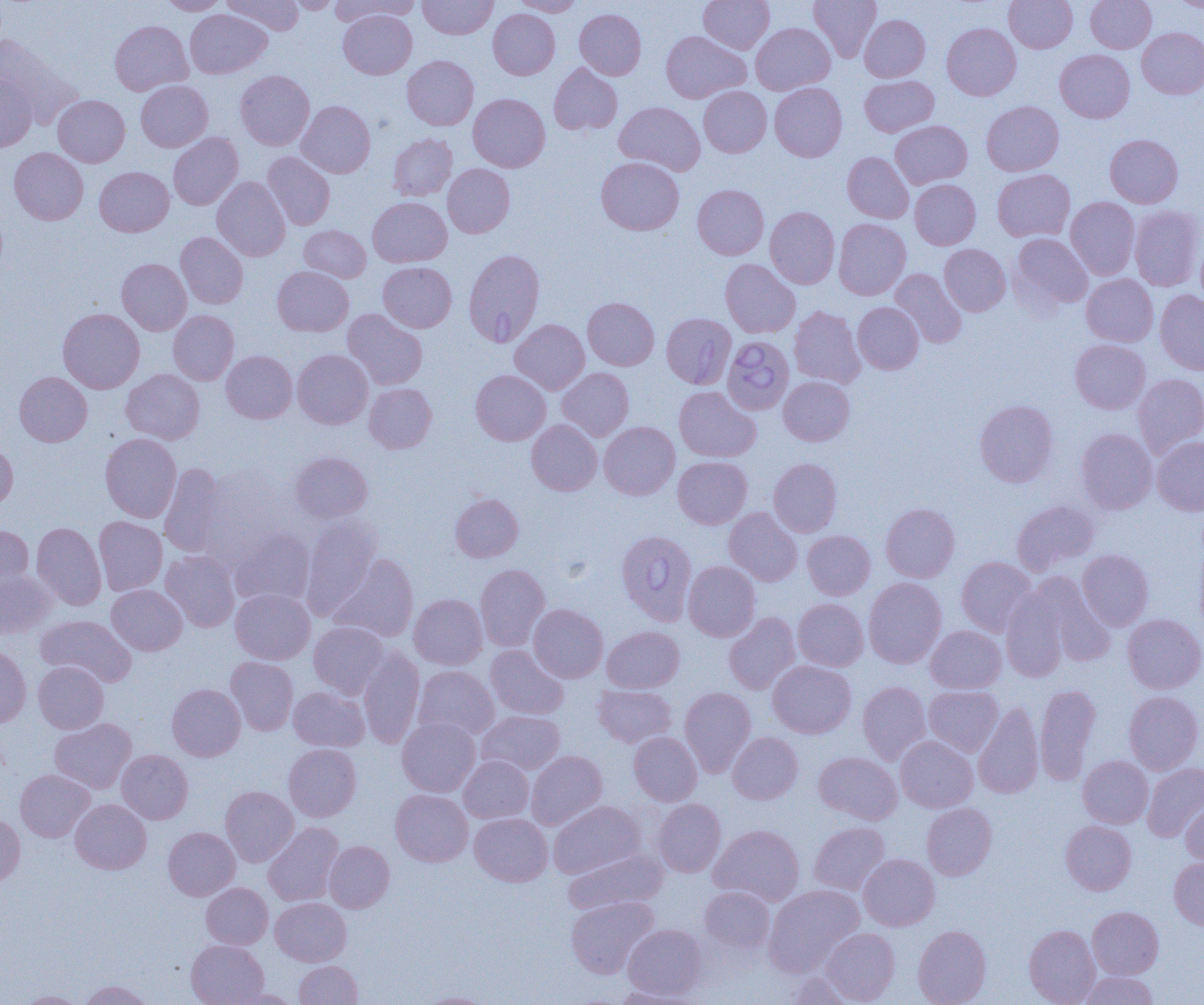
Approximate bounding boxes as [x1, y1, x2, y2] in pixels. Uninfected red blood cell locations: [160, 0, 227, 15], [222, 0, 304, 35], [285, 0, 341, 13], [330, 0, 421, 25], [418, 0, 498, 39], [512, 0, 583, 16], [698, 0, 774, 54], [809, 0, 881, 62], [1004, 0, 1077, 53], [1086, 0, 1156, 53], [1172, 0, 1204, 12], [185, 9, 271, 79], [488, 9, 560, 79], [574, 9, 646, 79], [338, 10, 417, 79], [860, 14, 930, 82], [110, 20, 193, 96], [751, 23, 835, 94], [942, 23, 1021, 100], [1137, 27, 1204, 99], [661, 31, 750, 103], [0, 33, 81, 128], [1055, 49, 1135, 123], [402, 55, 479, 130], [549, 63, 622, 135], [235, 70, 314, 150], [0, 74, 37, 152], [859, 75, 938, 136], [136, 80, 212, 152], [769, 83, 847, 161], [698, 86, 771, 157], [468, 93, 550, 172], [53, 95, 130, 167], [296, 100, 375, 178], [614, 101, 705, 175], [982, 101, 1064, 176], [890, 120, 972, 188], [168, 132, 243, 210], [388, 134, 457, 201], [1105, 134, 1183, 208], [9, 147, 88, 225], [262, 152, 335, 230], [842, 152, 913, 223], [596, 156, 684, 235], [443, 164, 515, 238], [94, 166, 174, 237], [992, 168, 1075, 242], [212, 176, 290, 261], [910, 179, 980, 249], [692, 184, 769, 259], [368, 197, 452, 267], [1066, 197, 1139, 279], [1129, 205, 1203, 291], [765, 206, 840, 289], [833, 218, 910, 300], [299, 225, 371, 282], [175, 232, 248, 309], [1010, 233, 1093, 312], [939, 244, 1011, 316], [117, 258, 191, 335], [720, 259, 800, 338], [378, 261, 457, 332], [272, 266, 353, 336], [890, 268, 967, 348], [1082, 274, 1158, 346], [1155, 290, 1204, 374], [582, 297, 659, 370], [853, 302, 923, 374], [789, 306, 866, 388], [58, 308, 144, 393], [342, 309, 427, 390], [168, 310, 238, 385], [510, 319, 590, 394], [1070, 339, 1150, 413], [292, 349, 373, 429], [221, 350, 297, 423], [557, 367, 633, 441], [121, 369, 205, 444], [471, 369, 550, 445], [14, 371, 92, 446], [1134, 373, 1204, 457], [779, 376, 855, 445], [364, 383, 437, 453], [674, 386, 760, 462], [975, 399, 1058, 487], [527, 420, 602, 495], [599, 421, 680, 499], [1076, 428, 1157, 514], [100, 434, 182, 522], [1152, 436, 1204, 516], [0, 440, 18, 511], [289, 451, 373, 524], [673, 456, 752, 529], [768, 458, 842, 537], [159, 462, 228, 558], [192, 464, 293, 563], [450, 493, 523, 562], [1012, 500, 1099, 575], [881, 503, 960, 582], [724, 507, 803, 586], [299, 514, 382, 619], [94, 517, 167, 595], [32, 521, 106, 610], [0, 524, 34, 596], [229, 528, 316, 607], [802, 530, 875, 599], [1077, 549, 1154, 630], [161, 551, 240, 631], [330, 553, 419, 642], [956, 556, 1037, 636], [683, 561, 760, 641], [475, 564, 550, 651], [0, 571, 55, 638], [1029, 573, 1115, 667], [863, 577, 947, 668], [107, 584, 187, 655], [231, 588, 315, 664], [1001, 588, 1069, 683], [409, 594, 487, 669], [792, 598, 868, 671], [528, 604, 608, 682], [724, 612, 801, 695], [1123, 614, 1204, 693], [36, 615, 136, 687], [308, 621, 390, 698], [926, 625, 1006, 693], [602, 626, 684, 693], [0, 644, 31, 729], [485, 645, 568, 720], [357, 647, 425, 749], [226, 657, 298, 735], [768, 660, 856, 738], [33, 661, 109, 733], [413, 666, 499, 743], [858, 681, 932, 764], [167, 684, 245, 761], [593, 684, 676, 748], [1035, 684, 1100, 785], [923, 685, 1003, 757], [288, 686, 369, 751], [679, 687, 756, 776], [1124, 690, 1203, 774], [974, 702, 1044, 799], [477, 710, 565, 775], [397, 716, 481, 796], [49, 718, 137, 794], [629, 731, 702, 805], [727, 732, 803, 804], [895, 735, 978, 812], [283, 743, 361, 821], [116, 749, 193, 824], [525, 750, 607, 830], [813, 751, 902, 824], [1078, 755, 1153, 828], [458, 756, 534, 823], [1142, 762, 1204, 841], [15, 769, 95, 842], [220, 786, 298, 866], [390, 789, 473, 866], [70, 799, 151, 874], [653, 799, 726, 877], [1181, 800, 1204, 868], [548, 801, 645, 879], [922, 803, 997, 880], [0, 813, 25, 888], [469, 813, 553, 886], [1060, 820, 1136, 895], [809, 821, 890, 896], [263, 822, 344, 906], [709, 824, 804, 906], [163, 827, 240, 900], [324, 841, 394, 913], [563, 847, 666, 913], [858, 854, 940, 931], [1169, 857, 1204, 931], [201, 883, 273, 949], [764, 884, 864, 975], [699, 886, 776, 953], [565, 896, 658, 978], [270, 897, 352, 966], [1087, 906, 1164, 979], [623, 923, 707, 999], [1024, 924, 1100, 1004], [913, 925, 991, 1005], [821, 927, 900, 1004], [186, 939, 268, 1005], [294, 960, 363, 1005], [785, 971, 858, 1005], [1077, 971, 1159, 1005], [80, 979, 151, 1005], [611, 986, 699, 1004], [227, 988, 301, 1004], [17, 991, 87, 1004], [419, 992, 494, 1005]. Babesia divergens-infected red blood cell locations: [464, 249, 545, 347], [661, 313, 736, 389], [722, 336, 794, 415], [616, 530, 697, 625]. Slide-level diagnosis: Babesia divergens. Single field of view. Thin blood smear. Light microscopy. Captured at 1000x magnification. Image is 1204×1005 pixels.